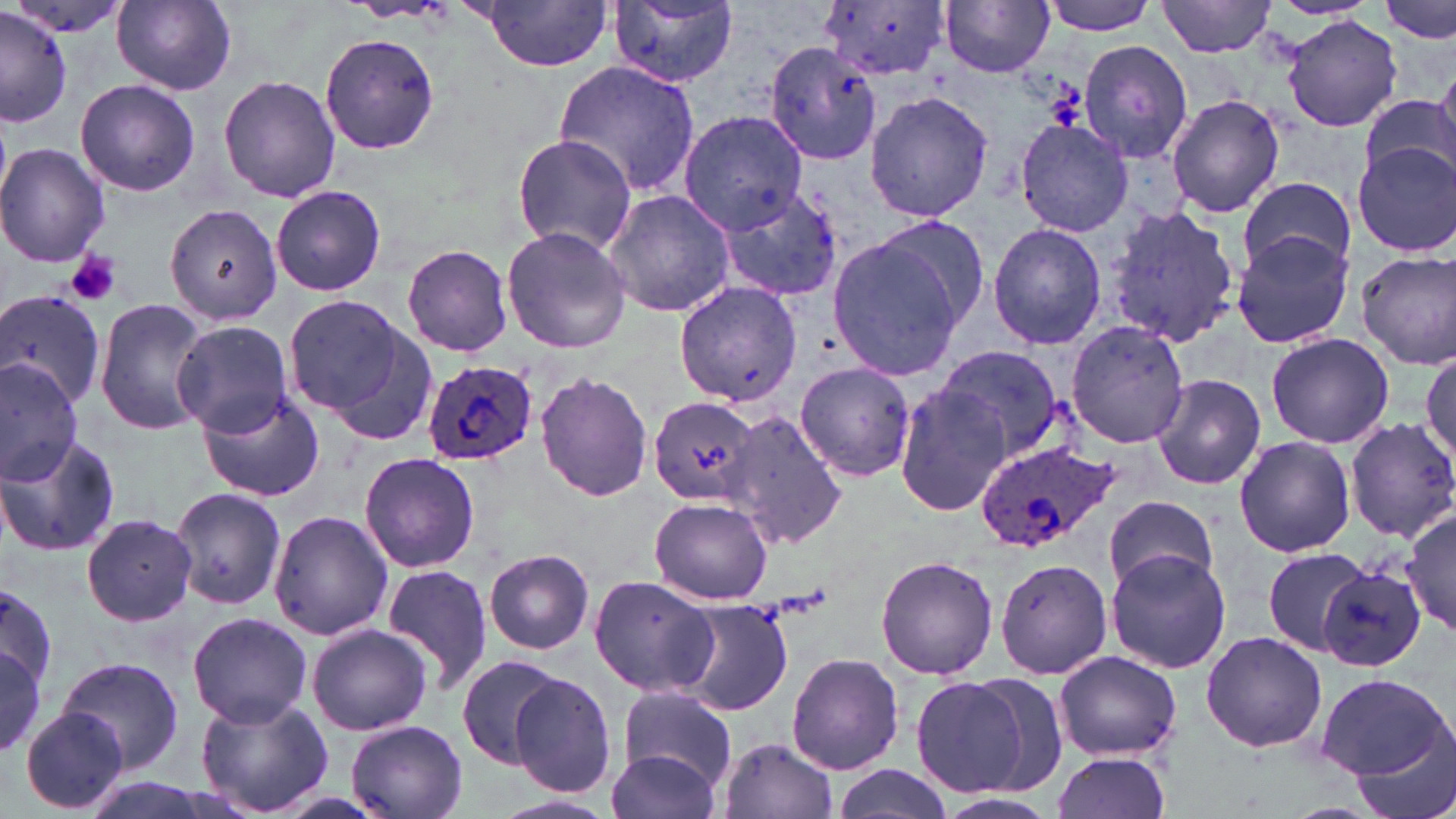
slide-level diagnosis = Plasmodium ovale
platelet locations = approximate bounding boxes as (x1,y1)-(x2,y2) corner pairs in pixels: (64,249)-(122,307)
image size = 1456×819 pixels
field of view = single
preparation = thin blood smear
Plasmodium ovale-infected red blood cell locations = approximate bounding boxes as (x1,y1)-(x2,y2) corner pairs in pixels: (424,361)-(539,466), (971,438)-(1118,552)
modality = light microscopy
stain = May-Grünwald-Giemsa
uninfected red blood cell locations = approximate bounding boxes as (x1,y1)-(x2,y2) corner pairs in pixels: (818,0)-(950,83), (1039,0)-(1162,35), (1158,0)-(1277,57), (1380,0)-(1455,44), (112,1)-(237,94), (940,1)-(1056,77), (3,2)-(134,40), (474,2)-(613,72), (609,3)-(738,88), (0,7)-(74,127), (1282,16)-(1400,132), (321,32)-(440,153), (765,38)-(883,167), (1078,40)-(1194,164), (552,61)-(702,197), (1430,69)-(1456,174), (219,73)-(341,204), (75,79)-(200,197), (865,91)-(991,222), (1360,91)-(1456,191), (1165,93)-(1285,217), (679,110)-(807,232), (1014,119)-(1134,238), (512,134)-(637,255), (1352,141)-(1456,258), (0,143)-(109,267), (1240,176)-(1355,277), (711,183)-(844,300), (271,184)-(386,296), (602,189)-(736,319), (166,205)-(284,327), (1105,206)-(1239,348), (869,217)-(989,330), (987,222)-(1106,351), (502,225)-(632,354), (1231,231)-(1355,350), (826,236)-(964,384), (402,245)-(512,356), (1356,250)-(1456,369), (674,282)-(802,407), (0,287)-(107,410), (95,298)-(212,435), (288,298)-(429,430), (172,320)-(295,435), (1064,320)-(1190,448), (1265,332)-(1393,450), (938,344)-(1064,462), (1421,345)-(1455,477), (0,357)-(81,486), (793,360)-(918,481), (535,371)-(654,503), (1151,375)-(1267,491), (892,383)-(1015,519), (198,391)-(327,503), (649,397)-(761,504), (725,407)-(845,549), (1343,415)-(1456,542), (0,430)-(121,558), (1234,434)-(1356,558), (357,450)-(480,573), (171,485)-(288,609), (1105,493)-(1218,594), (649,498)-(774,604), (1402,507)-(1456,633), (270,512)-(393,643), (82,513)-(197,626), (1264,545)-(1375,653), (484,549)-(595,654), (1106,551)-(1232,674), (876,553)-(998,680), (994,556)-(1113,679), (1315,562)-(1428,671), (382,566)-(499,699), (588,575)-(720,698), (0,578)-(61,703), (680,601)-(794,716), (187,611)-(313,726), (306,624)-(433,736), (1200,630)-(1328,753), (0,643)-(45,759), (1053,649)-(1181,762), (786,651)-(901,773), (457,654)-(567,768), (54,657)-(183,777), (964,670)-(1070,796), (1313,671)-(1450,780), (508,673)-(618,798), (911,676)-(1033,797), (618,684)-(737,793), (193,690)-(333,819), (22,707)-(128,814), (344,719)-(468,819), (1351,730)-(1456,819), (716,736)-(838,819), (607,745)-(724,819), (1050,750)-(1171,819), (828,764)-(954,819), (931,791)-(1063,819), (492,792)-(621,818)
magnification = 1000x